Outline each uninfected red blood cell.
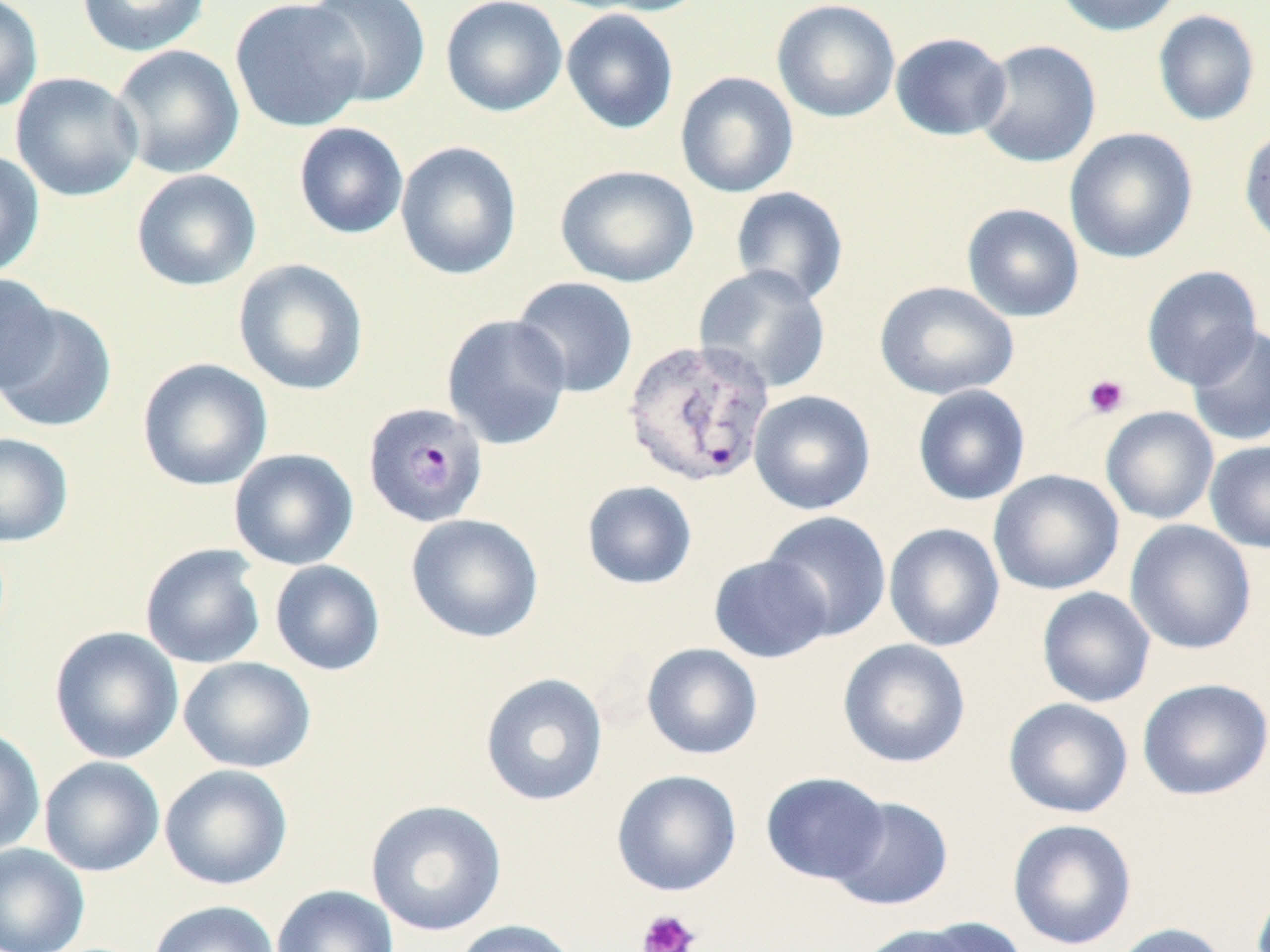
Approximate bounding boxes as [x1, y1, x2, y2] in pixels.
Uninfected red blood cells: [0, 0, 43, 113], [75, 0, 212, 58], [229, 0, 371, 133], [303, 0, 432, 107], [440, 0, 567, 118], [578, 0, 712, 17], [771, 0, 901, 123], [1052, 0, 1185, 37], [560, 9, 680, 134], [1152, 10, 1260, 126], [890, 32, 1012, 141], [974, 40, 1102, 168], [110, 44, 245, 179], [674, 71, 799, 198], [10, 72, 144, 202], [293, 122, 409, 239], [1238, 126, 1270, 251], [1064, 127, 1198, 264], [395, 141, 523, 281], [0, 150, 46, 279], [555, 164, 699, 287], [131, 169, 262, 291], [730, 186, 849, 306], [961, 203, 1084, 322], [233, 258, 369, 396], [693, 264, 831, 394], [1141, 265, 1263, 389], [0, 274, 60, 394], [510, 275, 638, 398], [874, 280, 1019, 400], [0, 302, 117, 433], [441, 313, 572, 450], [1186, 324, 1270, 447], [136, 357, 273, 491], [912, 384, 1031, 506], [749, 389, 876, 515], [1100, 406, 1219, 524], [0, 432, 74, 547], [1205, 441, 1270, 553], [228, 448, 359, 570], [988, 469, 1124, 595], [581, 480, 698, 590], [761, 510, 892, 641], [406, 513, 544, 643], [1124, 519, 1257, 655], [884, 522, 1005, 652], [139, 543, 267, 669], [708, 554, 834, 664], [270, 560, 385, 676], [1036, 586, 1156, 708], [49, 626, 184, 764], [837, 638, 971, 769], [641, 642, 763, 760], [178, 656, 317, 773], [479, 673, 608, 807], [1137, 678, 1270, 801], [1003, 697, 1134, 818], [0, 726, 45, 857], [39, 756, 165, 877], [159, 764, 293, 890], [611, 769, 742, 896], [760, 772, 890, 885], [827, 796, 954, 912], [364, 799, 507, 937], [1007, 818, 1138, 950], [0, 842, 90, 952], [271, 884, 399, 952], [148, 900, 280, 952], [913, 916, 1030, 952], [449, 919, 581, 952], [1108, 922, 1233, 952], [856, 923, 980, 952].

Platelet locations: [1082, 374, 1130, 420], [637, 909, 700, 952]. Plasmodium vivax-infected red blood cell locations: [620, 338, 776, 488], [363, 401, 489, 527]. Slide-level diagnosis: Plasmodium vivax. Light microscopy. Image is 1270×952 pixels. Single field of view. 1000x magnification. Thin blood film. May-Grünwald-Giemsa-stained preparation.